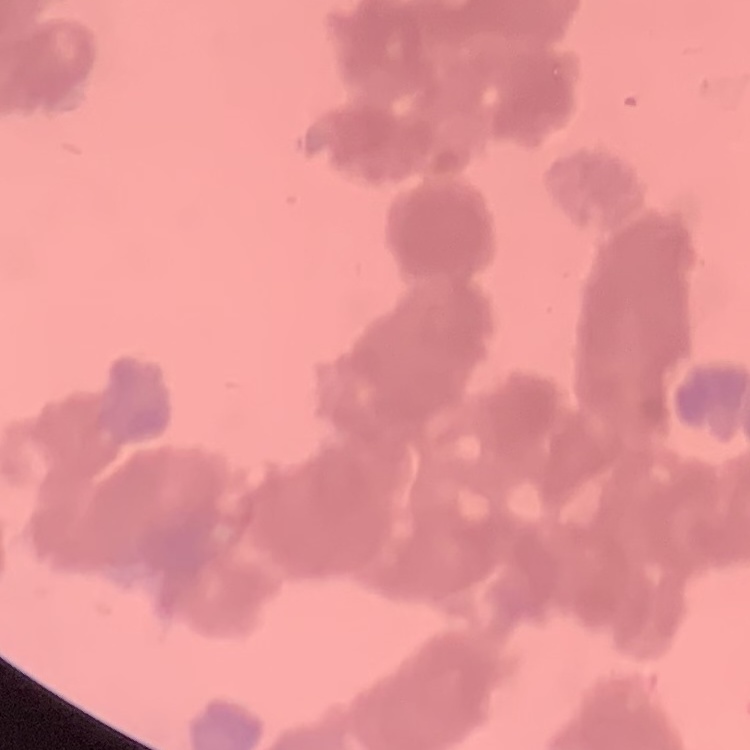 The red blood cells exhibit rouleaux formation. Stained with either Field's or Giemsa. Square crop of a larger photomicrograph. Thin blood smear.